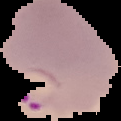

Summary:
  - Image size: 121×121 pixels
  - Preparation: thin blood film
  - Image type: segmented cell region on a black background
  - Result: malaria parasites identified